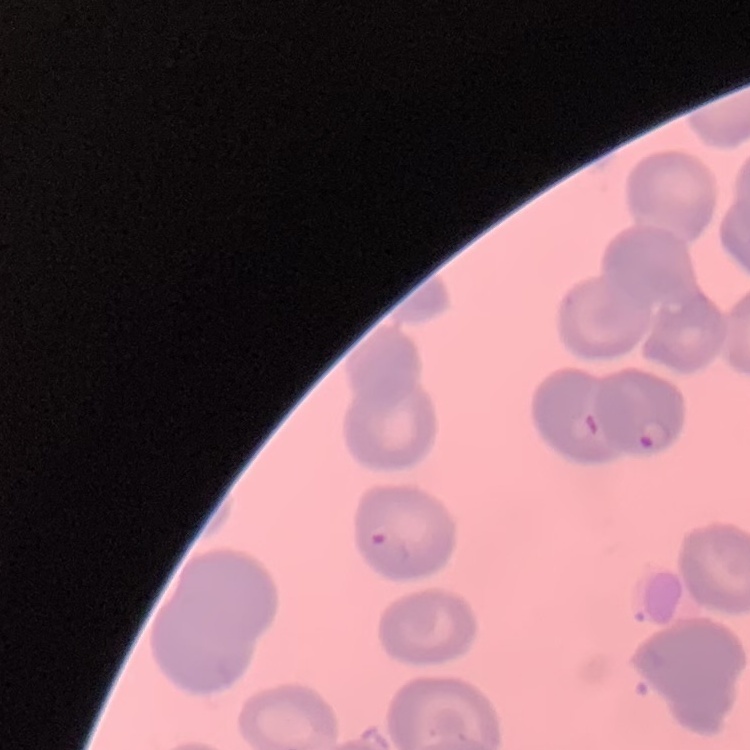
red_blood_cell_morphology: no rouleaux formation
preparation: thin peripheral smear
stain: Field's or Giemsa
image_type: square crop of a larger photomicrograph